Assess for malaria.
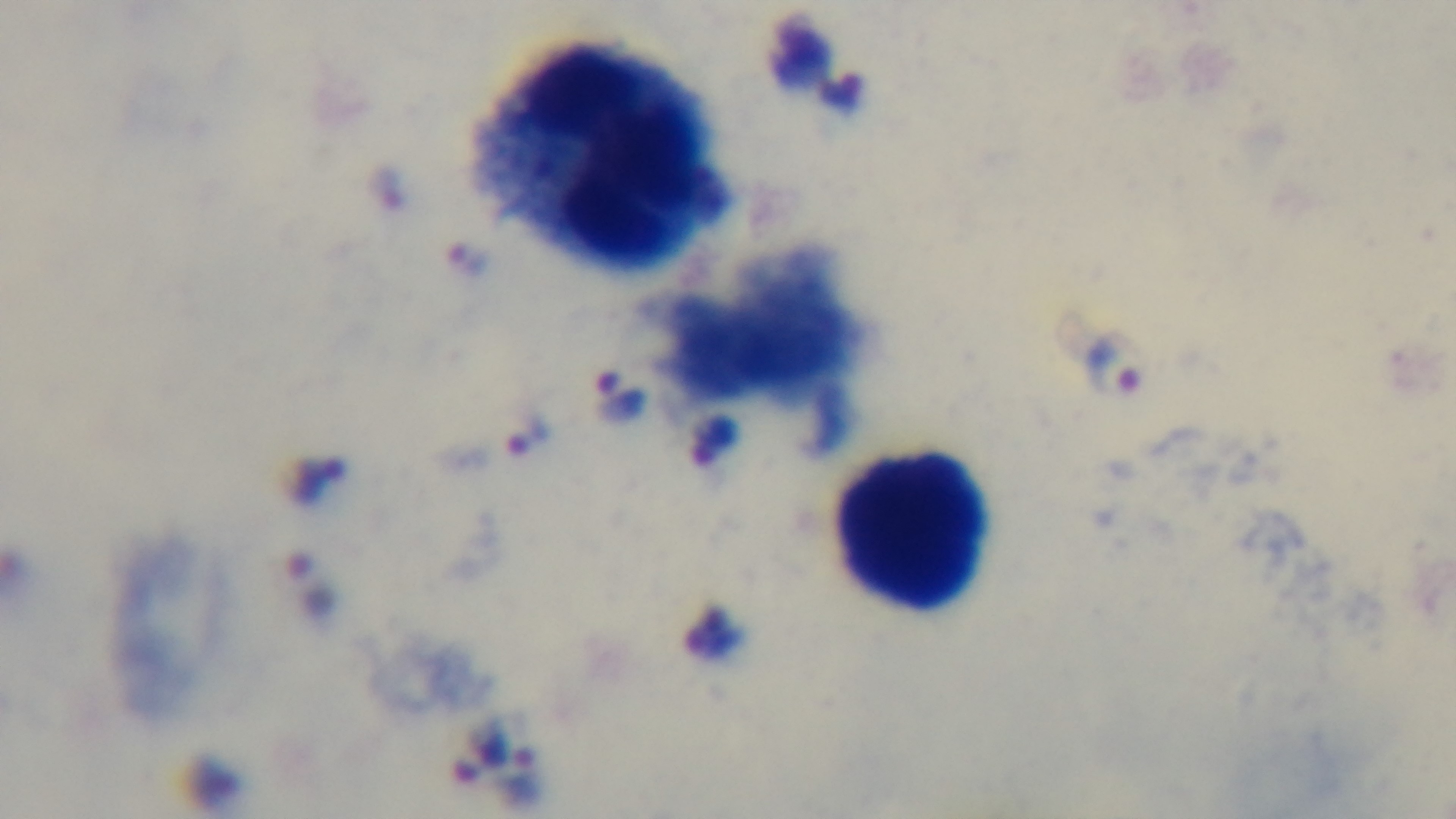

It is infected.

Summary:
  - Field of view: single
  - Preparation: thick smear
  - Capture: mounted 4K digital camera
  - Stain: Giemsa
  - Objective: 100x oil immersion
  - Modality: light microscopy